State which parasite is depicted.
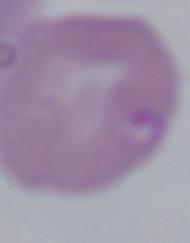
Babesia.

Summary:
  - Magnification: 1000x
  - Modality: micrograph